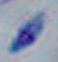

Toxoplasma gondii is seen. 1000x magnification. Micrograph.